Report the malaria status of this cell.
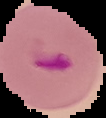

Parasitized.

Image is 106×118 pixels. The area outside the segmented cell region is set to black. From a thin blood smear.